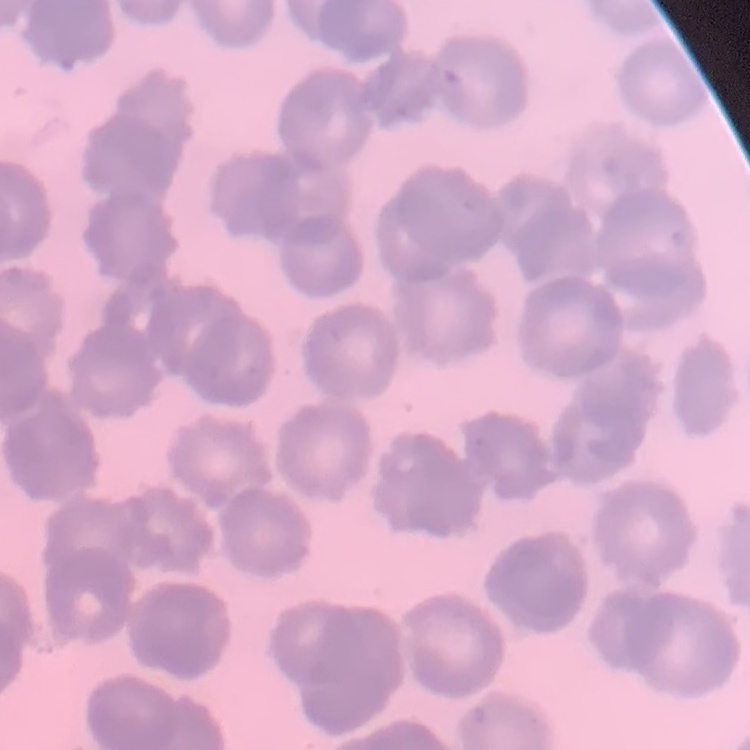
The erythrocytes exhibit rouleaux formation. Stained with either Field's or Giemsa. Square crop of a larger photomicrograph. Thin peripheral smear.